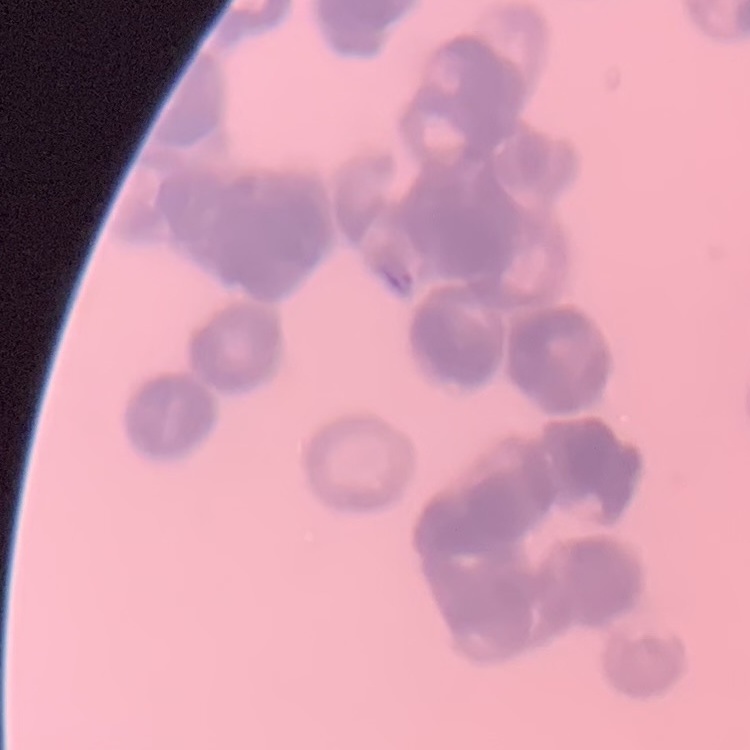 The erythrocytes show rouleaux formation. Thin peripheral smear. One tile cut from a larger photomicrograph. Field's or Giemsa stain.